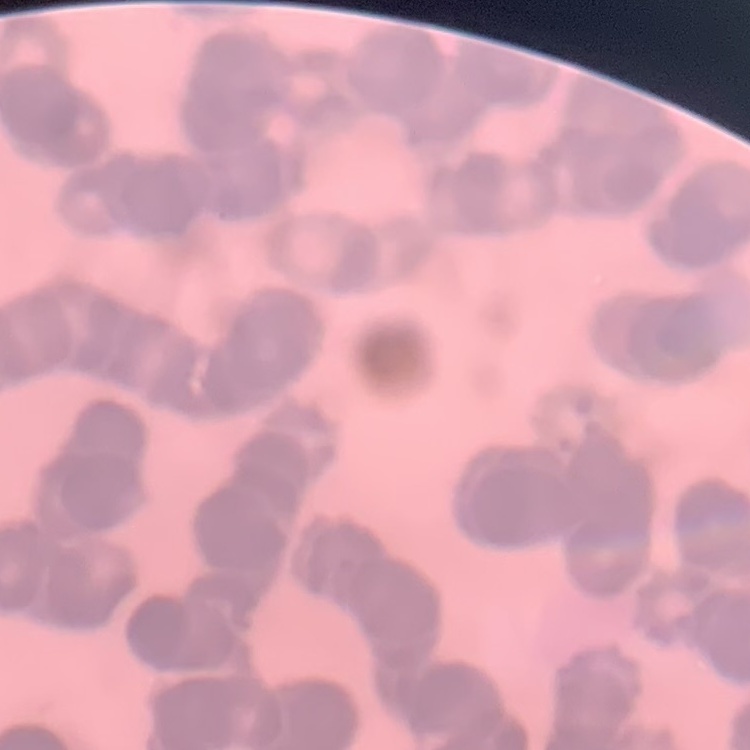

The red blood cells show rouleaux formation. Thin blood smear. Square crop of a larger photomicrograph. Stained with either Field's or Giemsa.